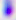
Toxoplasma gondii is shown. Photomicrograph. Captured at 400x magnification.